Report the malaria status of this cell.
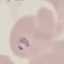
It is parasitized.

Summary:
  - Stain: Giemsa
  - Preparation: thin blood film
  - Image type: automatically extracted cell patch, resized to 64 × 64 pixels
  - Capture: smartphone camera at the microscope eyepiece